Classify this cell by malaria status.
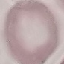
Uninfected.

Summary:
  - Capture: smartphone through the microscope eyepiece
  - Preparation: thin smear
  - Stain: Giemsa
  - Image type: automatically extracted cell patch, resized to 64 × 64 pixels